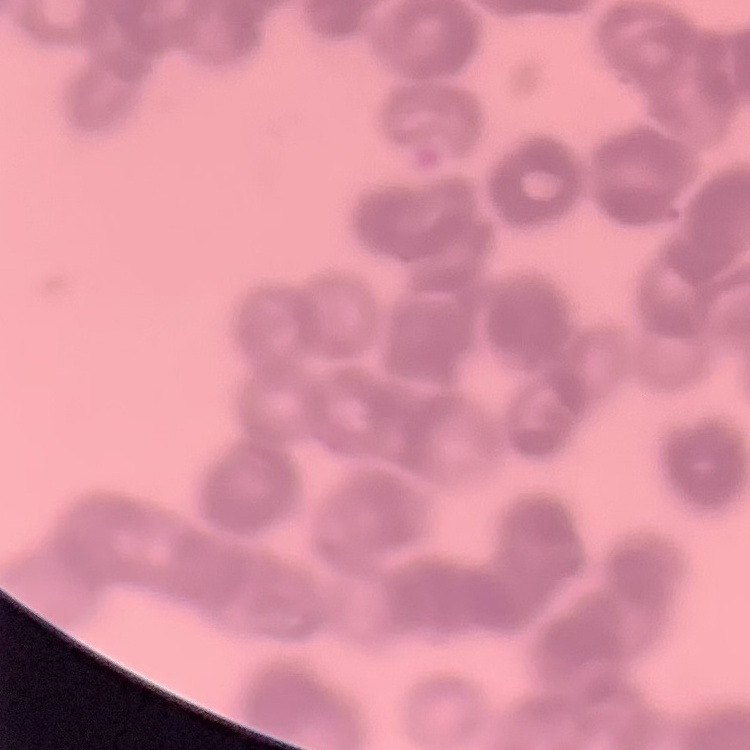
Summary:
  - Erythrocyte morphology: rouleaux formation
  - Stain: Field's or Giemsa
  - Preparation: thin blood film
  - Image type: one tile cut from a larger photomicrograph